State which cell type is depicted.
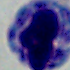

A leukocyte.

Summary:
  - Magnification: 1000x
  - Modality: micrograph